Name the cell type shown.
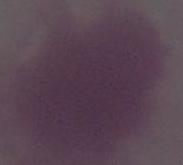

An erythrocyte.

Summary:
  - Modality: photomicrograph
  - Magnification: 1000x